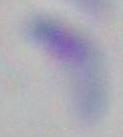
magnification = 1000x
identification = Toxoplasma gondii
modality = micrograph